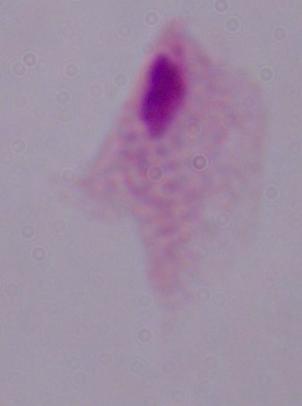

modality = micrograph
identification = trichomonad
magnification = 1000x